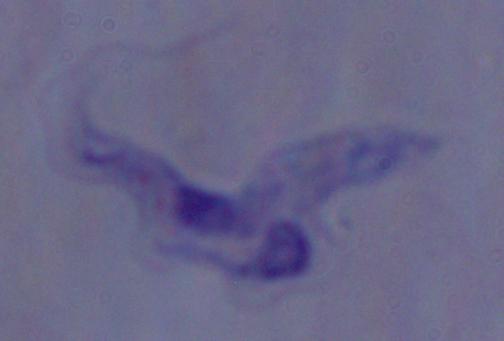
Summary:
  - Magnification: 1000x
  - Modality: photomicrograph
  - Identification: trypanosome